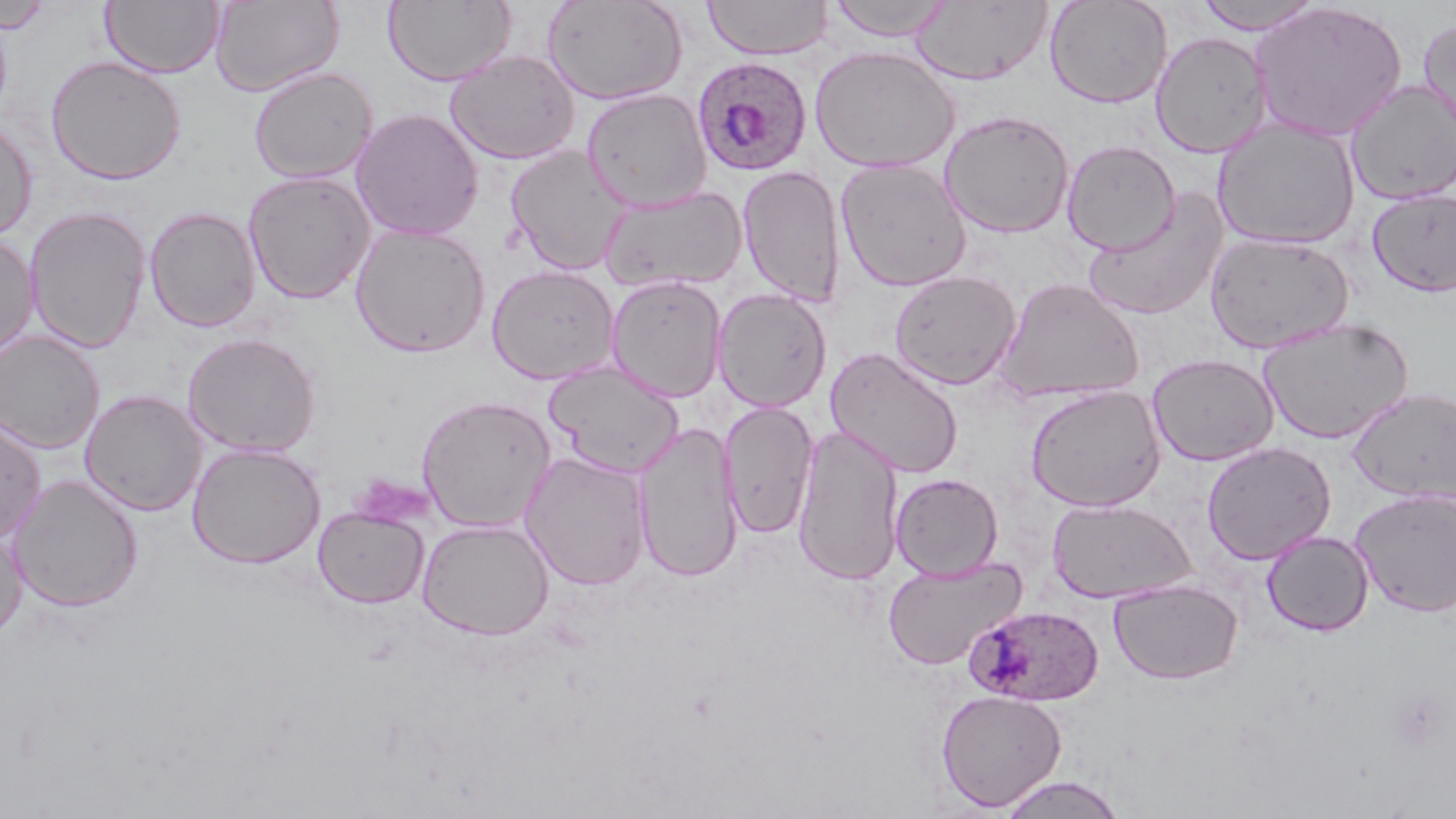

slide-level diagnosis = Plasmodium ovale
image size = 1456×819 pixels
field of view = single
uninfected red blood cell locations = approximate bounding boxes as (x1,y1)-(x2,y2) corner pairs in pixels: (1,0)-(54,34), (209,0)-(344,97), (383,0)-(516,87), (542,0)-(688,105), (703,0)-(833,60), (824,0)-(955,42), (1045,0)-(1173,109), (1192,0)-(1327,34), (101,1)-(225,78), (912,2)-(1053,84), (1249,2)-(1408,142), (1418,15)-(1456,141), (1151,31)-(1273,157), (809,45)-(960,176), (444,49)-(580,165), (46,55)-(187,185), (249,66)-(377,184), (1346,79)-(1456,205), (581,88)-(713,211), (350,108)-(484,241), (939,110)-(1075,238), (0,117)-(38,242), (1213,117)-(1360,250), (1062,140)-(1180,255), (505,145)-(633,275), (835,158)-(971,292), (738,165)-(847,306), (243,170)-(376,304), (599,185)-(749,293), (1083,189)-(1229,321), (1367,189)-(1456,297), (24,206)-(151,353), (144,206)-(260,333), (349,223)-(491,358), (1205,231)-(1355,354), (0,233)-(39,360), (486,264)-(620,384), (889,270)-(1021,390), (605,275)-(728,403), (995,277)-(1146,404), (712,288)-(832,413), (1257,317)-(1414,444), (0,330)-(105,454), (182,332)-(322,456), (825,347)-(964,479), (1147,353)-(1280,466), (544,361)-(684,478), (1025,384)-(1167,513), (1347,387)-(1456,504), (80,389)-(207,516), (416,394)-(556,532), (719,400)-(819,539), (0,416)-(46,544), (633,421)-(744,583), (793,424)-(904,586), (1201,441)-(1337,565), (186,442)-(326,569), (519,450)-(652,591), (891,472)-(1003,580), (7,473)-(144,613), (1350,488)-(1456,617), (1047,497)-(1196,604), (313,506)-(429,608), (417,518)-(554,640), (0,527)-(28,640), (1261,529)-(1374,636), (882,555)-(1027,670), (1109,579)-(1243,685), (936,689)-(1067,811), (996,774)-(1128,818)
stain = May-Grünwald-Giemsa
Plasmodium ovale-infected red blood cell locations = approximate bounding boxes as (x1,y1)-(x2,y2) corner pairs in pixels: (691,56)-(812,177), (963,604)-(1105,706)
preparation = thin blood smear
modality = light microscopy
magnification = 1000x
platelet locations = approximate bounding boxes as (x1,y1)-(x2,y2) corner pairs in pixels: (1387,688)-(1450,752)